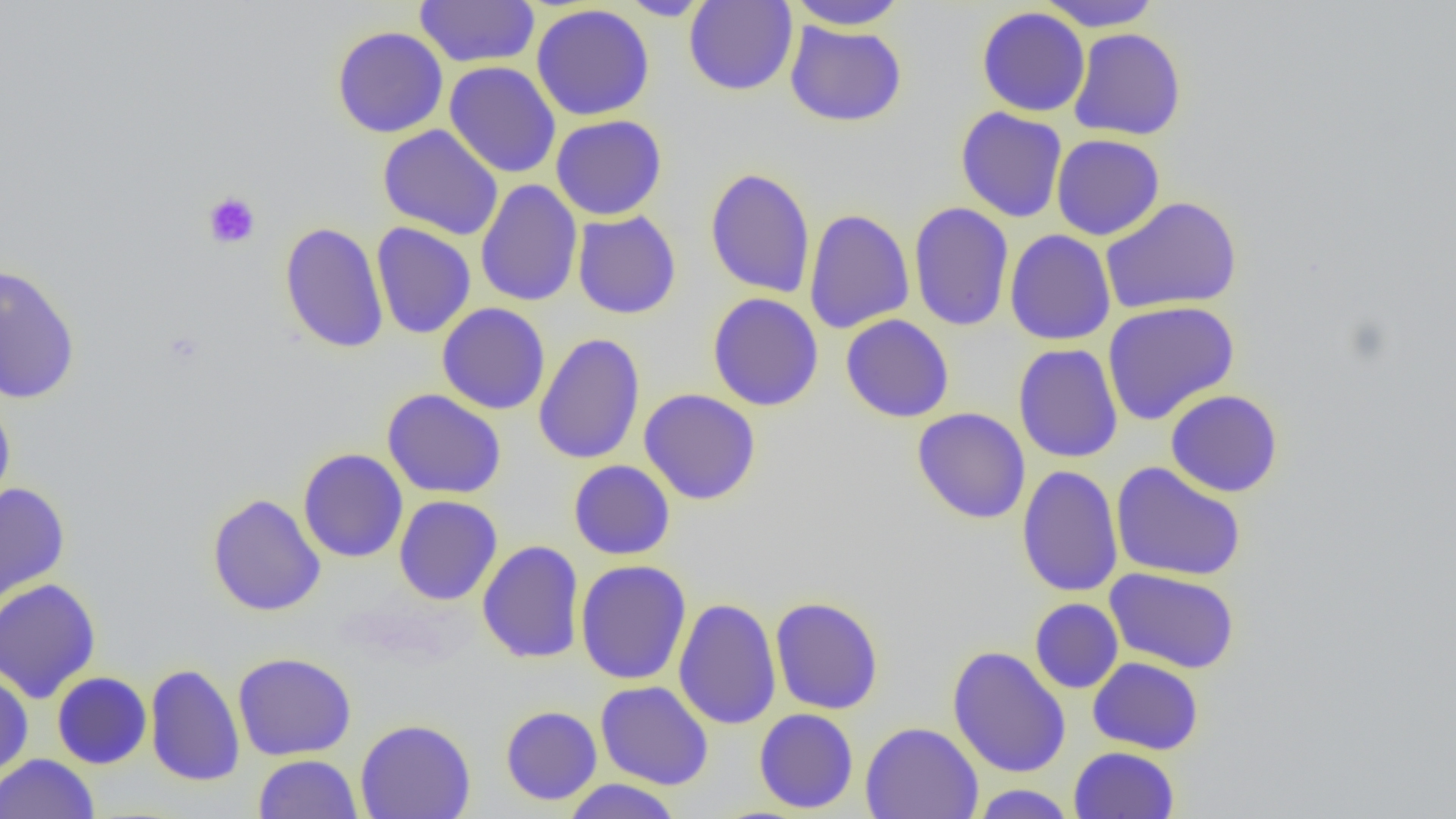

Approximate bounding boxes as named x1/y1/x2/y2 corners in pixels. Uninfected red blood cell locations: (x1=414, y1=0, x2=540, y2=68), (x1=683, y1=0, x2=798, y2=96), (x1=1036, y1=0, x2=1161, y2=31), (x1=618, y1=1, x2=713, y2=20), (x1=785, y1=1, x2=910, y2=30), (x1=531, y1=4, x2=654, y2=121), (x1=976, y1=6, x2=1091, y2=117), (x1=784, y1=21, x2=907, y2=127), (x1=332, y1=26, x2=448, y2=138), (x1=1068, y1=27, x2=1187, y2=141), (x1=444, y1=61, x2=561, y2=178), (x1=955, y1=106, x2=1068, y2=223), (x1=550, y1=114, x2=667, y2=220), (x1=377, y1=124, x2=504, y2=241), (x1=1051, y1=134, x2=1165, y2=240), (x1=704, y1=167, x2=816, y2=298), (x1=475, y1=179, x2=583, y2=307), (x1=1100, y1=196, x2=1242, y2=314), (x1=908, y1=201, x2=1014, y2=332), (x1=804, y1=208, x2=914, y2=335), (x1=572, y1=211, x2=681, y2=319), (x1=279, y1=222, x2=389, y2=354), (x1=371, y1=222, x2=476, y2=339), (x1=1004, y1=229, x2=1116, y2=345), (x1=0, y1=262, x2=82, y2=405), (x1=707, y1=292, x2=824, y2=411), (x1=1101, y1=301, x2=1240, y2=425), (x1=437, y1=302, x2=551, y2=415), (x1=841, y1=314, x2=954, y2=423), (x1=532, y1=333, x2=646, y2=465), (x1=1013, y1=343, x2=1123, y2=463), (x1=382, y1=389, x2=507, y2=499), (x1=639, y1=389, x2=761, y2=505), (x1=1165, y1=389, x2=1283, y2=497), (x1=0, y1=397, x2=16, y2=517), (x1=912, y1=407, x2=1031, y2=524), (x1=298, y1=448, x2=409, y2=563), (x1=568, y1=460, x2=675, y2=560), (x1=1110, y1=461, x2=1246, y2=581), (x1=1017, y1=464, x2=1123, y2=597), (x1=0, y1=482, x2=70, y2=607), (x1=207, y1=493, x2=326, y2=617), (x1=394, y1=495, x2=502, y2=605), (x1=477, y1=540, x2=585, y2=664), (x1=575, y1=560, x2=691, y2=684), (x1=1104, y1=567, x2=1240, y2=674), (x1=0, y1=578, x2=101, y2=703), (x1=770, y1=595, x2=884, y2=715), (x1=673, y1=597, x2=782, y2=731), (x1=1030, y1=598, x2=1124, y2=693), (x1=947, y1=645, x2=1071, y2=778), (x1=232, y1=652, x2=357, y2=760), (x1=1087, y1=656, x2=1204, y2=755), (x1=145, y1=663, x2=245, y2=786), (x1=0, y1=670, x2=33, y2=779), (x1=52, y1=671, x2=152, y2=769), (x1=595, y1=681, x2=713, y2=790), (x1=500, y1=705, x2=602, y2=806), (x1=754, y1=708, x2=859, y2=813), (x1=355, y1=718, x2=476, y2=819), (x1=860, y1=721, x2=983, y2=819), (x1=1069, y1=746, x2=1180, y2=818), (x1=0, y1=753, x2=99, y2=819), (x1=253, y1=754, x2=362, y2=818), (x1=562, y1=778, x2=682, y2=818), (x1=969, y1=784, x2=1078, y2=818). Platelet locations: (x1=202, y1=191, x2=261, y2=250). Slide-level diagnosis: no evidence of blood parasites. Captured at 1000x magnification. One field of a larger specimen. Thin blood smear. Optical microscopy. Image is 1456×819 pixels.